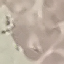

result = no malaria parasites seen
stain = Giemsa
preparation = thin blood film
image type = cell patch, automatically extracted from a larger field of view and resized to 64 × 64 pixels
capture = smartphone through the microscope eyepiece